Assess for Plasmodium parasites.
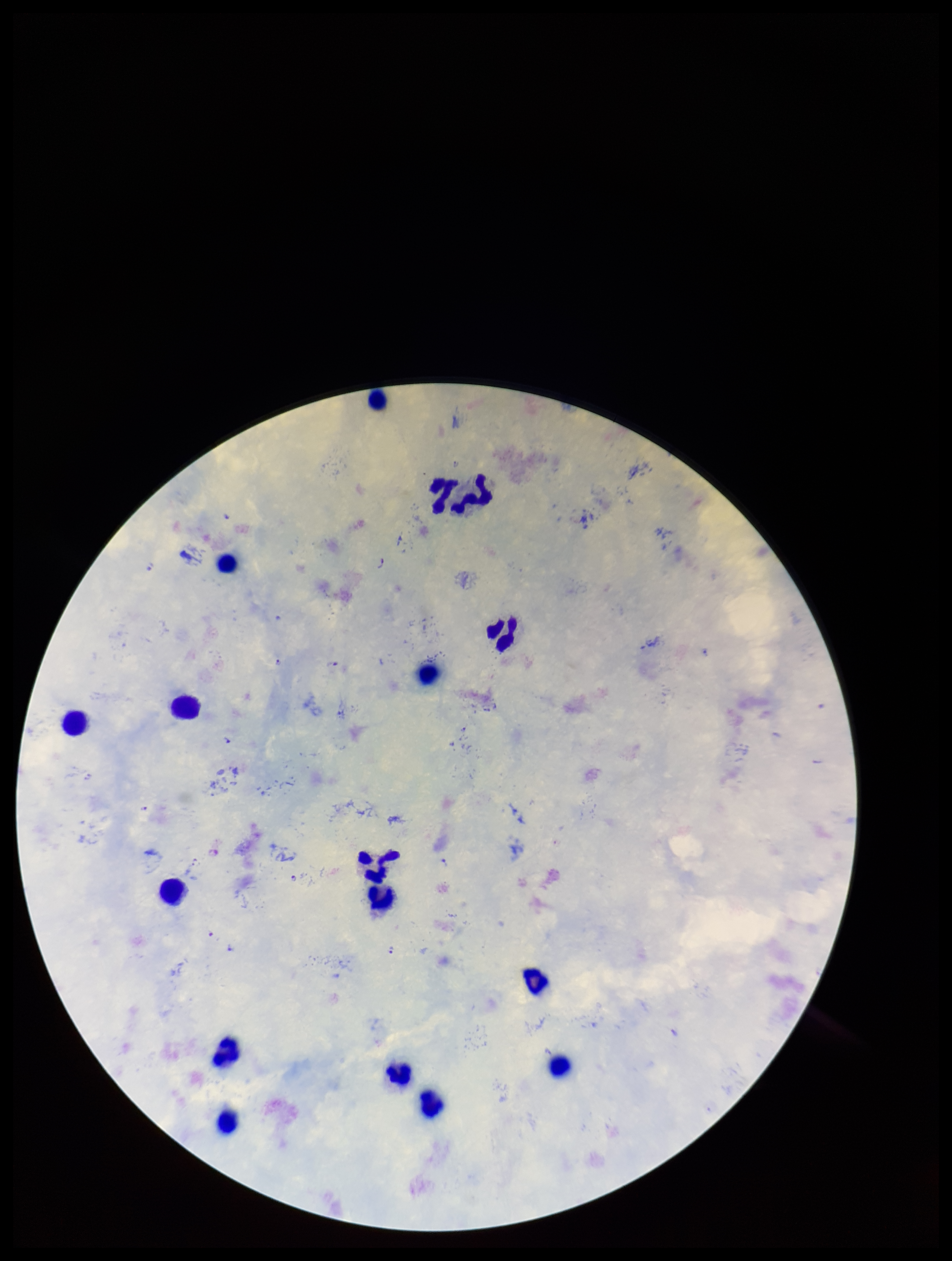
Identified.

patient malaria status = positive
image size = 952×1261 pixels
parasite count = 8
field of view = single
species reported for this patient = Plasmodium falciparum
preparation = thick smear
leukocyte count = 17
stain = Giemsa
capture = smartphone photograph through the microscope eyepiece